Name the cell type shown.
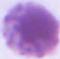
This is an erythrocyte.

Photomicrograph. Captured at 1000x magnification.